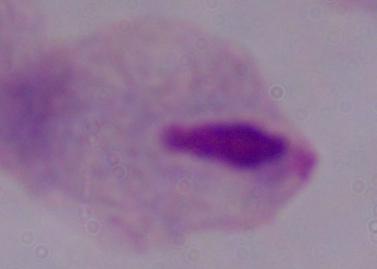

magnification = 1000x
modality = photomicrograph
identification = trichomonad